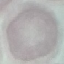

result: negative for malaria parasites
stain: Giemsa
image_type: automatically extracted cell patch, resized to 64 × 64 pixels
preparation: thin smear
capture: smartphone camera at the microscope eyepiece